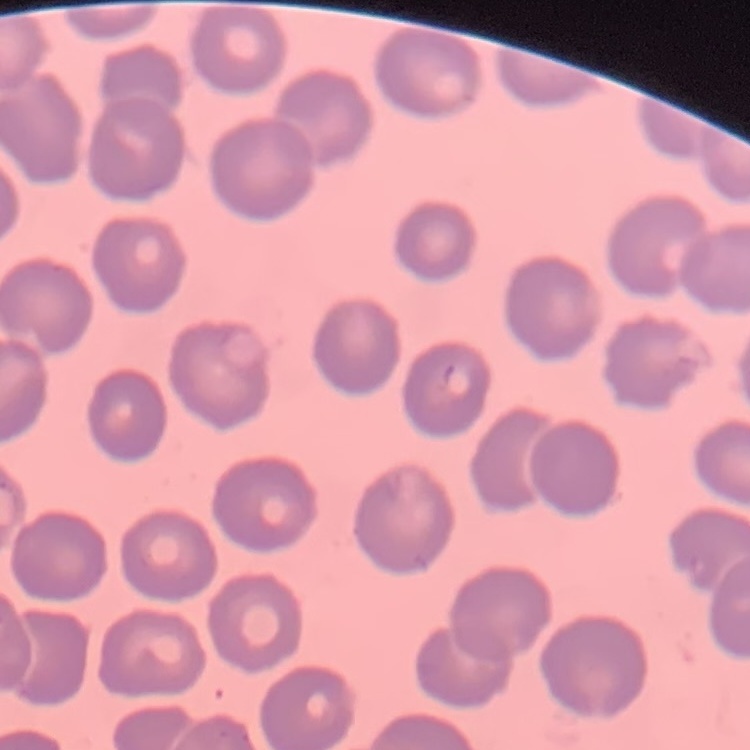

The red blood cells exhibit no rouleaux formation. Square crop of a larger photomicrograph. Thin blood film. Stained with either Field's or Giemsa.